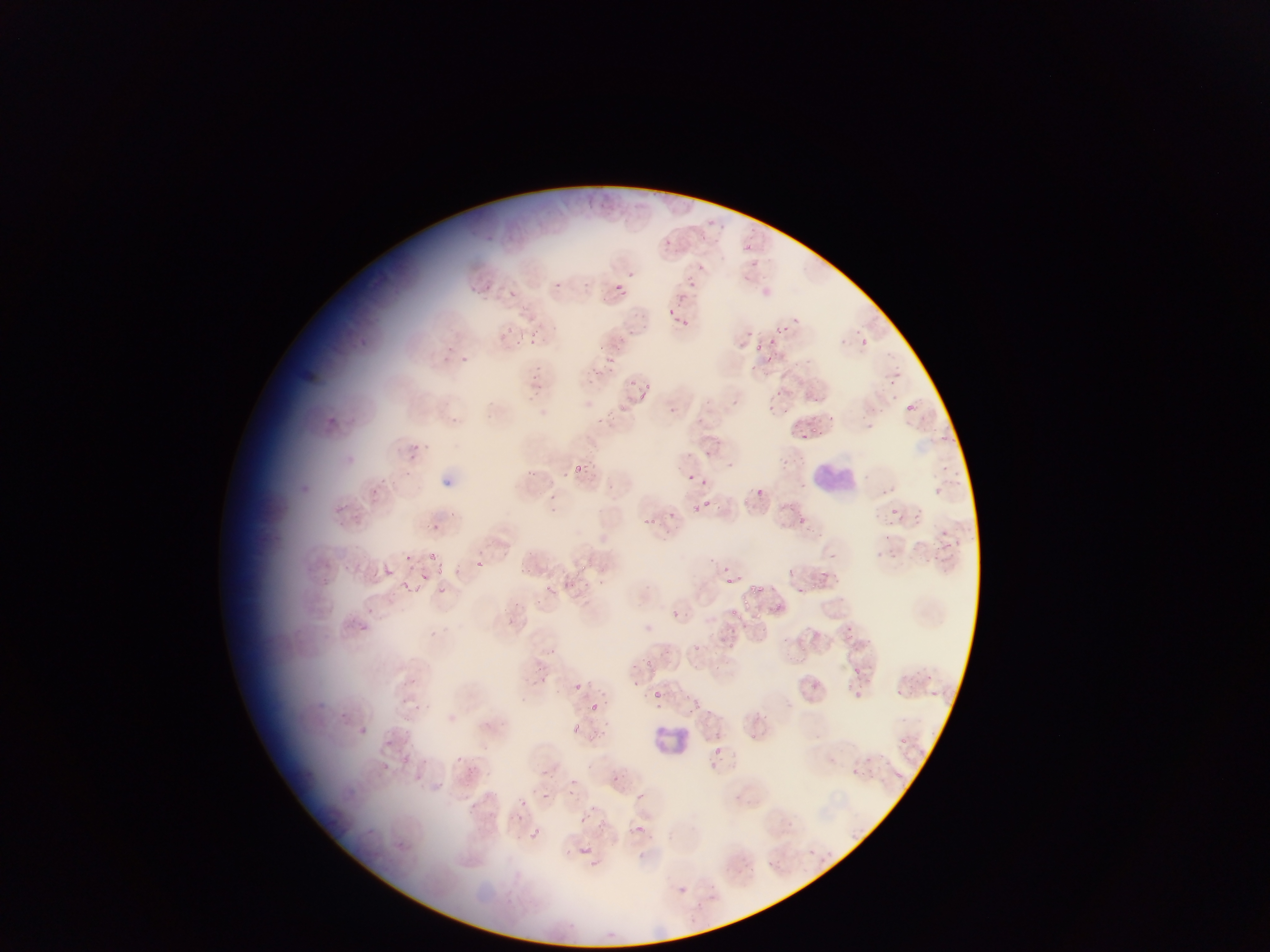

Approximate bounding boxes as {left, top, right, bottom} in pixels.
Summary:
  - Leukocyte locations: {901, 400, 920, 417}, {809, 456, 863, 501}, {797, 514, 808, 532}, {656, 724, 691, 759}, {713, 745, 722, 760}
  - Plasmodium parasite locations: {707, 217, 719, 229}, {717, 221, 729, 234}, {662, 237, 673, 249}, {742, 244, 753, 255}, {695, 262, 706, 274}, {483, 277, 494, 289}, {615, 277, 629, 295}, {688, 280, 709, 302}, {553, 281, 577, 306}, {509, 287, 519, 301}, {668, 307, 679, 318}, {677, 319, 690, 336}, {499, 323, 514, 337}, {549, 323, 561, 334}, {779, 324, 796, 338}, {853, 326, 865, 338}, {744, 329, 757, 336}, {529, 330, 538, 352}, {836, 336, 845, 347}, {615, 338, 635, 352}, {859, 338, 868, 347}, {754, 339, 774, 359}, {445, 340, 458, 357}, {462, 354, 476, 370}, {601, 354, 614, 366}, {582, 362, 598, 378}, {537, 364, 548, 372}, {748, 366, 757, 375}, {893, 368, 906, 375}, {529, 371, 540, 381}, {626, 376, 640, 390}, {888, 378, 897, 389}, {588, 379, 594, 387}, {640, 379, 652, 394}, {774, 388, 786, 399}, {814, 392, 826, 406}, {731, 398, 742, 412}, {666, 403, 685, 421}, {767, 405, 774, 417}, {611, 412, 623, 419}, {828, 412, 838, 419}, {323, 414, 346, 439}, {597, 415, 610, 426}, {865, 418, 877, 430}, {809, 424, 821, 439}, {938, 429, 951, 444}, {413, 442, 433, 461}, {684, 447, 691, 461}, {705, 447, 717, 459}, {726, 458, 742, 465}, {943, 459, 954, 474}, {572, 463, 586, 479}, {405, 468, 420, 485}, {527, 468, 543, 480}, {560, 471, 569, 481}, {374, 473, 389, 484}, {688, 473, 697, 484}, {702, 477, 711, 492}, {369, 485, 382, 503}, {938, 485, 952, 498}, {757, 487, 768, 499}, {548, 490, 557, 502}, {702, 500, 717, 509}, {689, 501, 700, 514}, {547, 505, 559, 515}, {333, 506, 353, 518}, {889, 506, 909, 528}, {444, 509, 460, 520}, {665, 509, 676, 518}, {641, 514, 653, 524}, {431, 523, 440, 530}, {942, 524, 956, 541}, {661, 527, 672, 538}, {880, 533, 892, 542}, {888, 549, 904, 563}, {929, 549, 946, 564}, {428, 550, 444, 565}, {403, 552, 415, 566}, {582, 558, 598, 574}, {723, 558, 733, 573}, {473, 560, 487, 569}, {387, 564, 399, 578}, {787, 564, 797, 577}, {520, 565, 539, 580}, {819, 566, 831, 578}, {437, 569, 452, 575}, {739, 570, 748, 577}, {419, 571, 430, 583}, {563, 574, 591, 598}, {402, 576, 416, 589}, {725, 578, 733, 586}, {543, 580, 557, 595}, {754, 582, 771, 597}, {798, 584, 807, 593}, {439, 585, 446, 593}, {741, 596, 753, 613}, {668, 609, 681, 620}, {506, 616, 518, 625}, {353, 620, 373, 637}, {846, 623, 860, 636}, {428, 628, 442, 637}, {692, 641, 712, 665}, {541, 643, 553, 656}, {642, 655, 659, 676}, {531, 659, 547, 671}, {849, 664, 863, 677}, {407, 676, 423, 688}, {539, 676, 546, 685}, {572, 682, 584, 693}, {891, 687, 910, 698}, {852, 690, 863, 700}, {653, 691, 660, 703}, {690, 696, 709, 715}, {586, 697, 601, 713}, {568, 721, 585, 737}, {379, 739, 391, 747}, {456, 752, 468, 766}, {400, 754, 419, 768}, {849, 764, 866, 780}, {542, 766, 551, 777}, {610, 773, 621, 785}, {568, 778, 579, 790}, {541, 792, 551, 802}, {638, 792, 652, 803}, {520, 798, 530, 811}, {471, 800, 484, 814}, {593, 804, 600, 816}, {578, 813, 586, 821}, {635, 822, 646, 836}, {527, 824, 543, 840}, {362, 825, 379, 841}, {577, 844, 595, 855}, {591, 857, 605, 871}, {681, 883, 692, 895} | approximate {x, y} pixel centers of objects too small to bound: {362, 728}
  - Preparation: thin blood film
  - Country: Ghana
  - Image size: 1270×952 pixels
  - Field of view: single
  - Capture: mobile-phone photograph through a microscope